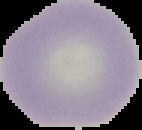

Summary:
  - Image type: segmented cell region on a black background
  - Malaria status: uninfected
  - Preparation: thin blood smear
  - Image size: 142×130 pixels